Assess this cell for malaria.
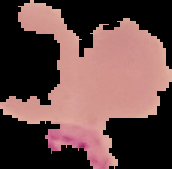

It is uninfected.

The area outside the segmented cell region is set to black. From a thin blood film. Image is 172×169 pixels.